State which parasite is depicted.
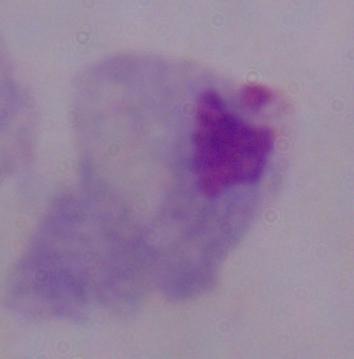
A trichomonad.

magnification = 1000x
modality = photomicrograph